Identify the parasite.
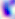
This is Toxoplasma gondii.

{
  "magnification": "400x",
  "modality": "micrograph"
}